Identify the blood parasite species.
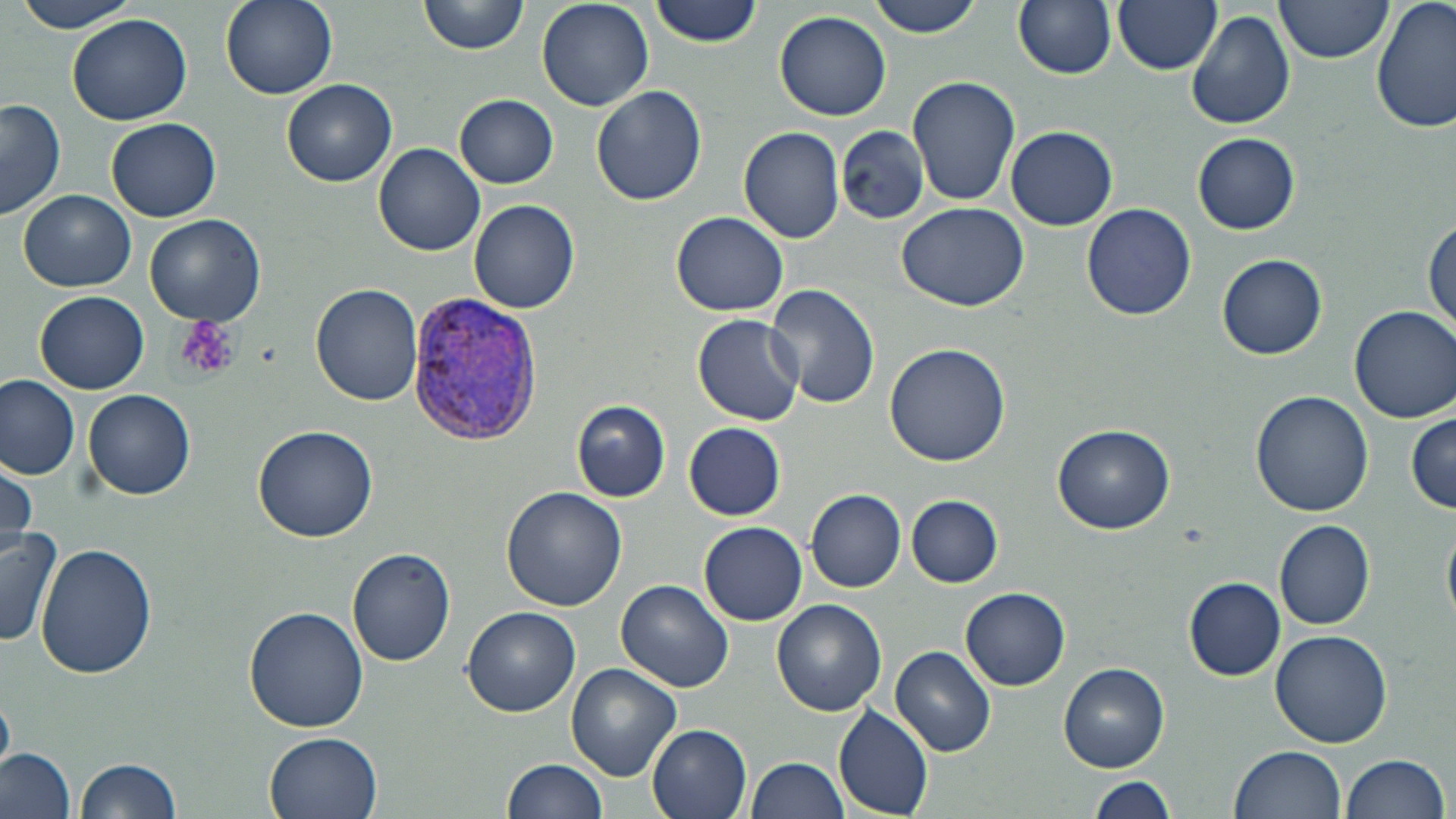

Plasmodium vivax.

image size = 1456×819 pixels
field of view = one of a larger specimen
modality = light microscopy
magnification = 1000x
stain = May-Grünwald-Giemsa
preparation = thin blood smear
Plasmodium vivax-infected red blood cell locations = approximate bounding boxes as (x1, y1, x2, y2) in pixels: (405, 296, 542, 440)
platelet locations = approximate bounding boxes as (x1, y1, x2, y2) in pixels: (175, 316, 241, 381)
uninfected red blood cell locations = approximate bounding boxes as (x1, y1, x2, y2) in pixels: (13, 0, 142, 33), (221, 0, 337, 99), (419, 0, 529, 56), (650, 0, 763, 47), (864, 0, 987, 38), (1012, 0, 1118, 79), (1113, 0, 1222, 75), (1275, 0, 1394, 63), (1372, 0, 1455, 134), (535, 1, 653, 110), (1187, 9, 1296, 130), (775, 10, 892, 121), (67, 14, 192, 126), (907, 75, 1021, 207), (282, 78, 396, 186), (592, 85, 707, 206), (455, 94, 558, 189), (0, 98, 65, 222), (107, 117, 220, 222), (1006, 125, 1118, 231), (737, 126, 846, 244), (836, 127, 930, 225), (1192, 134, 1299, 234), (374, 142, 486, 256), (19, 189, 135, 292), (468, 199, 581, 315), (897, 202, 1030, 311), (1081, 203, 1196, 320), (670, 211, 789, 316), (145, 214, 267, 326), (1425, 218, 1456, 335), (1217, 254, 1328, 359), (312, 282, 423, 406), (767, 284, 879, 409), (35, 289, 151, 394), (1350, 306, 1456, 423), (692, 314, 805, 425), (883, 342, 1010, 467), (0, 375, 80, 481), (83, 389, 197, 501), (1250, 389, 1375, 517), (571, 399, 671, 502), (1406, 411, 1456, 512), (683, 422, 786, 520), (689, 422, 794, 622), (1052, 424, 1175, 533), (253, 426, 379, 543), (1, 454, 38, 557), (501, 487, 629, 613), (807, 489, 906, 592), (905, 494, 1004, 587), (1443, 517, 1456, 632), (1273, 518, 1375, 629), (698, 521, 807, 625), (0, 527, 64, 646), (36, 543, 157, 679), (348, 546, 457, 666), (1184, 577, 1285, 680), (616, 579, 735, 692), (960, 586, 1071, 690), (772, 600, 887, 716), (461, 606, 581, 717), (244, 607, 367, 732), (1272, 630, 1393, 749), (891, 645, 996, 756), (1060, 662, 1169, 771), (566, 664, 682, 783), (0, 695, 14, 776), (833, 703, 934, 817), (646, 722, 752, 819), (265, 731, 384, 819), (1230, 745, 1346, 819), (0, 748, 76, 819), (1340, 753, 1451, 819), (77, 757, 184, 819), (503, 757, 608, 819), (747, 757, 850, 818), (1087, 777, 1179, 818)